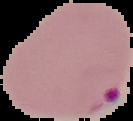 Result: malaria parasites detected. From a thin blood film. Image is 133×121 pixels. Segmented cell region on a black background.